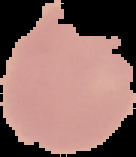
image_size: 136×157 pixels
image_type: cell region segmented out of the field of view; surrounding area masked to black
preparation: thin blood smear
result: no malaria parasites seen